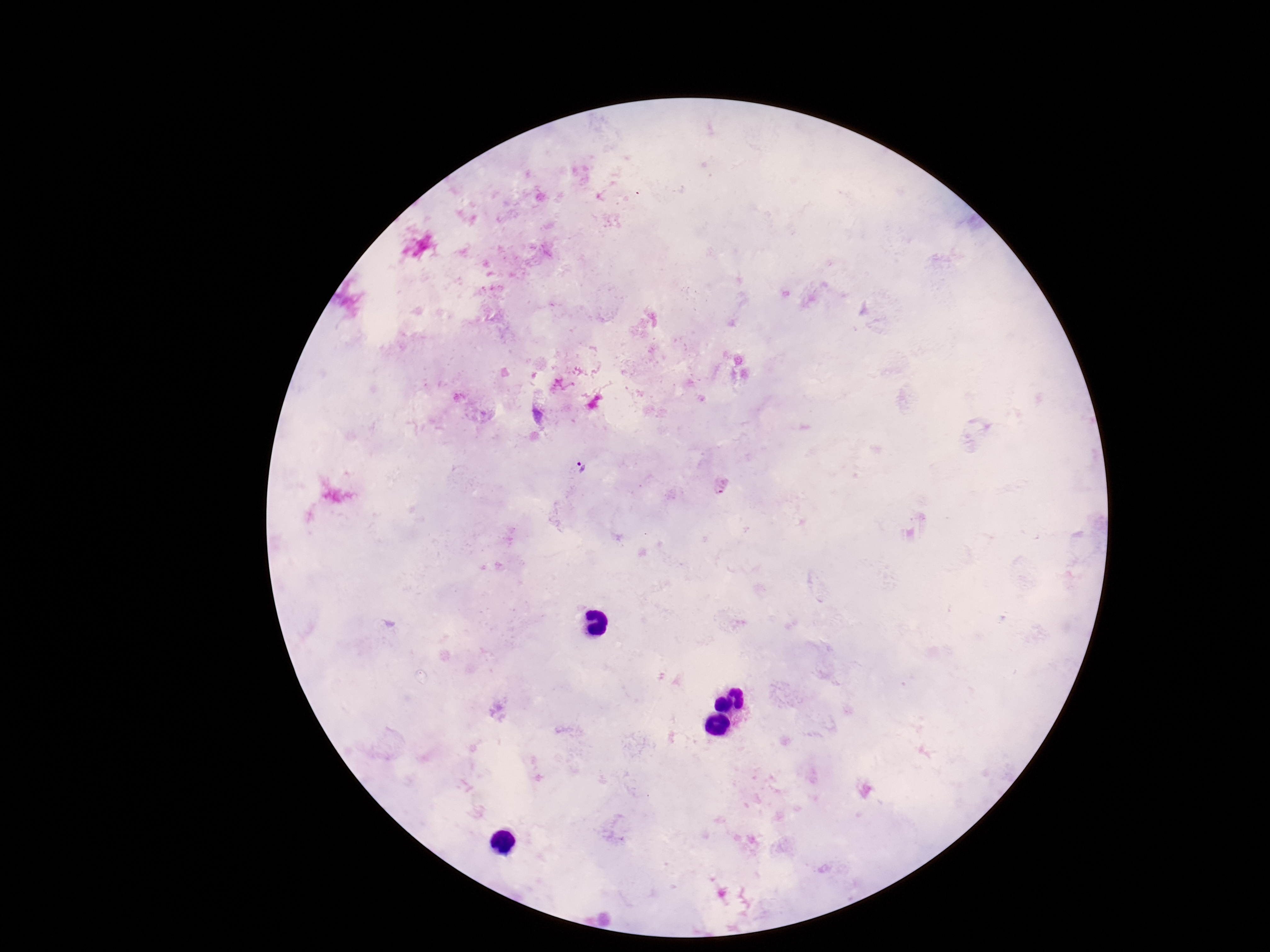
{
  "preparation": "thick blood film",
  "plasmodium_parasite_locations": "approximate object centers, in pixels from the top-left corner: (x=581, y=465)",
  "field_of_view": "one from this slide",
  "stain": "Giemsa",
  "patient_malaria_status": "infected",
  "capture": "smartphone camera through the microscope eyepiece",
  "image_size": "1270×952 pixels",
  "magnification": "100x"
}